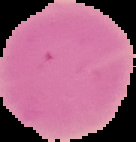
Malaria status: uninfected. Image is 136×142 pixels. From a thin blood smear. Cell region segmented out of the field of view; the surrounding area is masked to black.